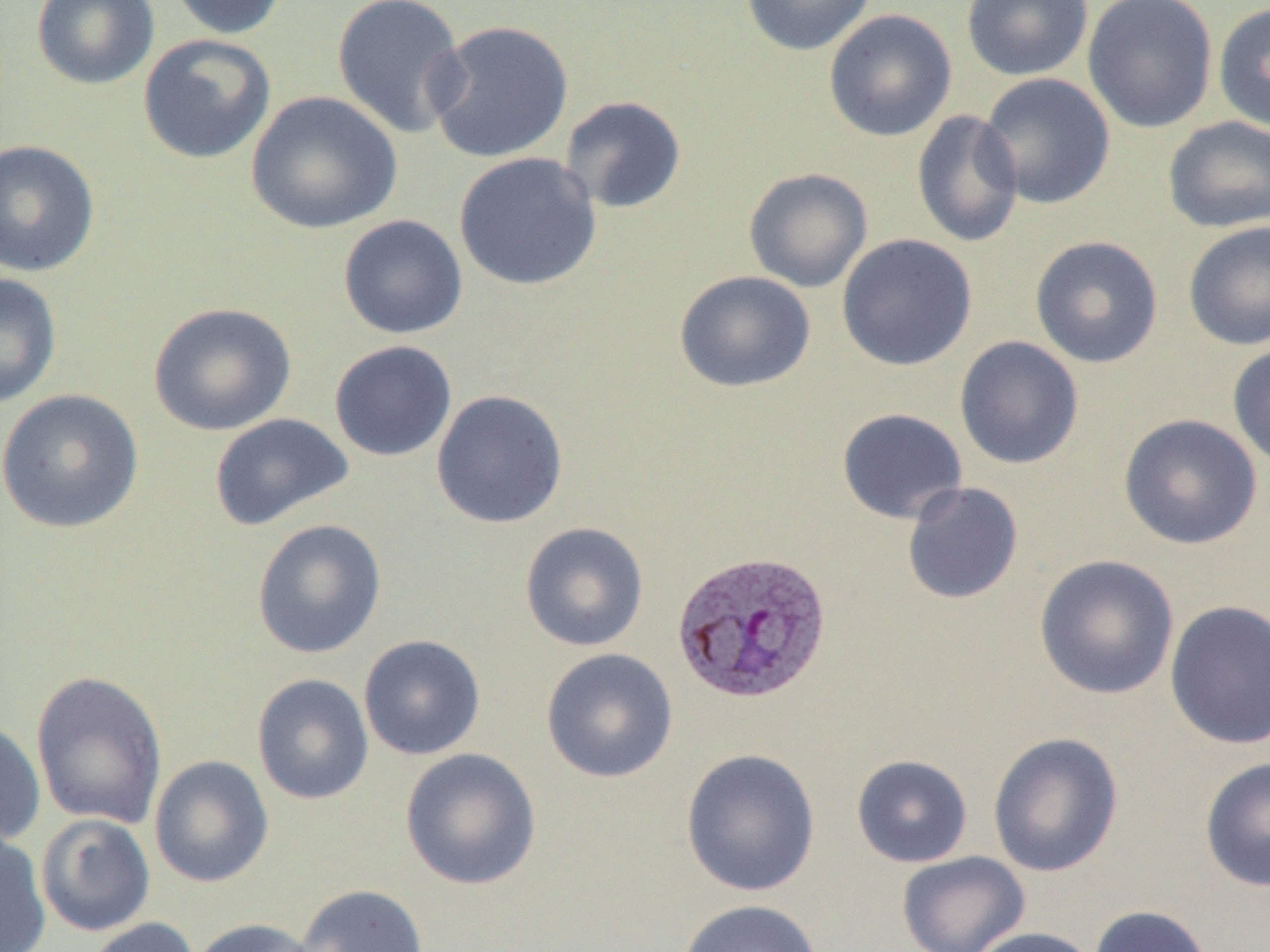

Summary:
  - Coordinate format: approximate bounding boxes as [x1, y1, x2, y2] in pixels
  - Plasmodium vivax-infected red blood cell locations: [670, 549, 833, 706]
  - Uninfected red blood cell locations: [31, 0, 159, 90], [165, 0, 290, 40], [331, 0, 469, 139], [739, 0, 878, 56], [961, 0, 1093, 81], [1082, 0, 1218, 134], [1213, 2, 1270, 133], [823, 9, 957, 142], [425, 19, 574, 163], [138, 34, 276, 164], [978, 73, 1115, 210], [245, 90, 402, 234], [559, 95, 687, 214], [911, 109, 1024, 248], [1162, 116, 1270, 233], [0, 139, 100, 277], [453, 152, 602, 291], [743, 168, 873, 293], [337, 214, 468, 339], [1182, 221, 1270, 351], [836, 234, 978, 372], [1029, 235, 1164, 369], [674, 270, 816, 393], [0, 272, 62, 409], [148, 301, 297, 437], [954, 336, 1084, 470], [328, 340, 457, 462], [1227, 341, 1270, 471], [0, 389, 145, 534], [430, 389, 569, 529], [836, 408, 968, 524], [209, 413, 354, 531], [1118, 414, 1263, 550], [901, 481, 1024, 604], [251, 519, 387, 659], [519, 521, 650, 652], [1034, 554, 1179, 700], [1165, 600, 1270, 750], [358, 634, 486, 761], [540, 648, 678, 783], [30, 670, 167, 829], [251, 673, 374, 805], [0, 719, 46, 848], [988, 731, 1123, 877], [400, 747, 542, 890], [680, 748, 821, 897], [851, 754, 973, 868], [148, 755, 274, 888], [1199, 756, 1270, 892], [36, 813, 156, 937], [0, 829, 51, 952], [896, 850, 1031, 952], [294, 883, 429, 952], [678, 899, 824, 952], [1088, 904, 1215, 952], [84, 917, 200, 952], [189, 918, 321, 952], [967, 926, 1101, 952]
  - Slide-level diagnosis: Plasmodium vivax
  - Modality: light microscopy
  - Magnification: 1000x
  - Image size: 1270×952 pixels
  - Preparation: thin blood film
  - Field of view: single